Give the extent of all Plasmodium falciparum-infected red blood cells.
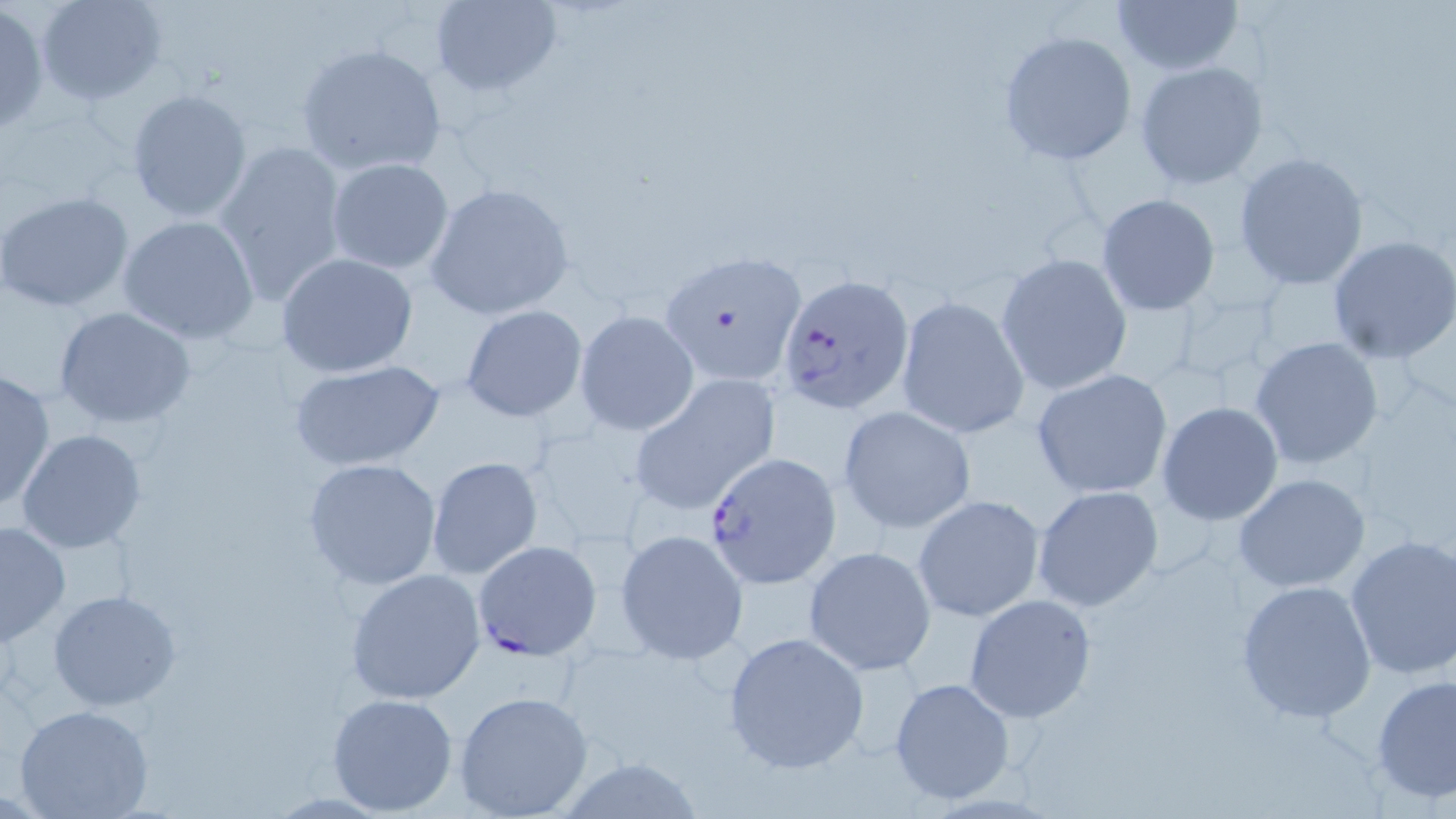
Approximate bounding boxes as (x1,y1)-(x2,y2) corner pairs in pixels.
Plasmodium falciparum-infected red blood cells: (778,273)-(915,415), (705,452)-(841,585), (471,540)-(600,659).

Uninfected red blood cell locations: (35,0)-(168,106), (1111,0)-(1243,76), (430,1)-(561,97), (0,5)-(48,133), (997,30)-(1137,165), (295,43)-(448,177), (1134,61)-(1270,191), (125,88)-(254,224), (213,139)-(349,308), (1233,153)-(1369,291), (325,157)-(453,275), (425,180)-(577,322), (0,191)-(135,314), (1096,193)-(1219,314), (117,215)-(261,343), (1327,235)-(1456,363), (657,248)-(805,386), (277,252)-(418,378), (996,253)-(1132,395), (895,297)-(1029,438), (461,306)-(587,422), (55,307)-(197,429), (575,309)-(699,435), (1249,337)-(1385,469), (290,358)-(449,472), (0,368)-(55,512), (1031,369)-(1174,499), (632,377)-(778,513), (1156,402)-(1284,526), (837,405)-(976,534), (16,427)-(148,553), (425,456)-(544,580), (302,457)-(443,591), (1233,474)-(1371,592), (1032,485)-(1165,612), (913,495)-(1045,622), (0,518)-(70,646), (613,529)-(748,664), (1344,531)-(1456,679), (803,546)-(935,675), (346,567)-(487,705), (1237,580)-(1377,723), (46,588)-(183,712), (963,594)-(1096,722), (723,631)-(869,774), (1371,672)-(1456,806), (889,677)-(1016,806), (453,690)-(595,818), (326,692)-(460,814), (14,705)-(154,819), (550,757)-(711,817). Slide-level diagnosis: Plasmodium falciparum. Thin blood smear. Optical microscopy. May-Grünwald-Giemsa-stained preparation. Single field of view. Image is 1456×819 pixels. Captured at 1000x magnification.